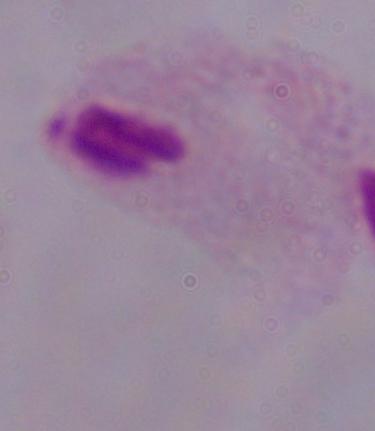
identification = trichomonad
magnification = 1000x
modality = photomicrograph